Outline each Plasmodium ovale-infected red blood cell.
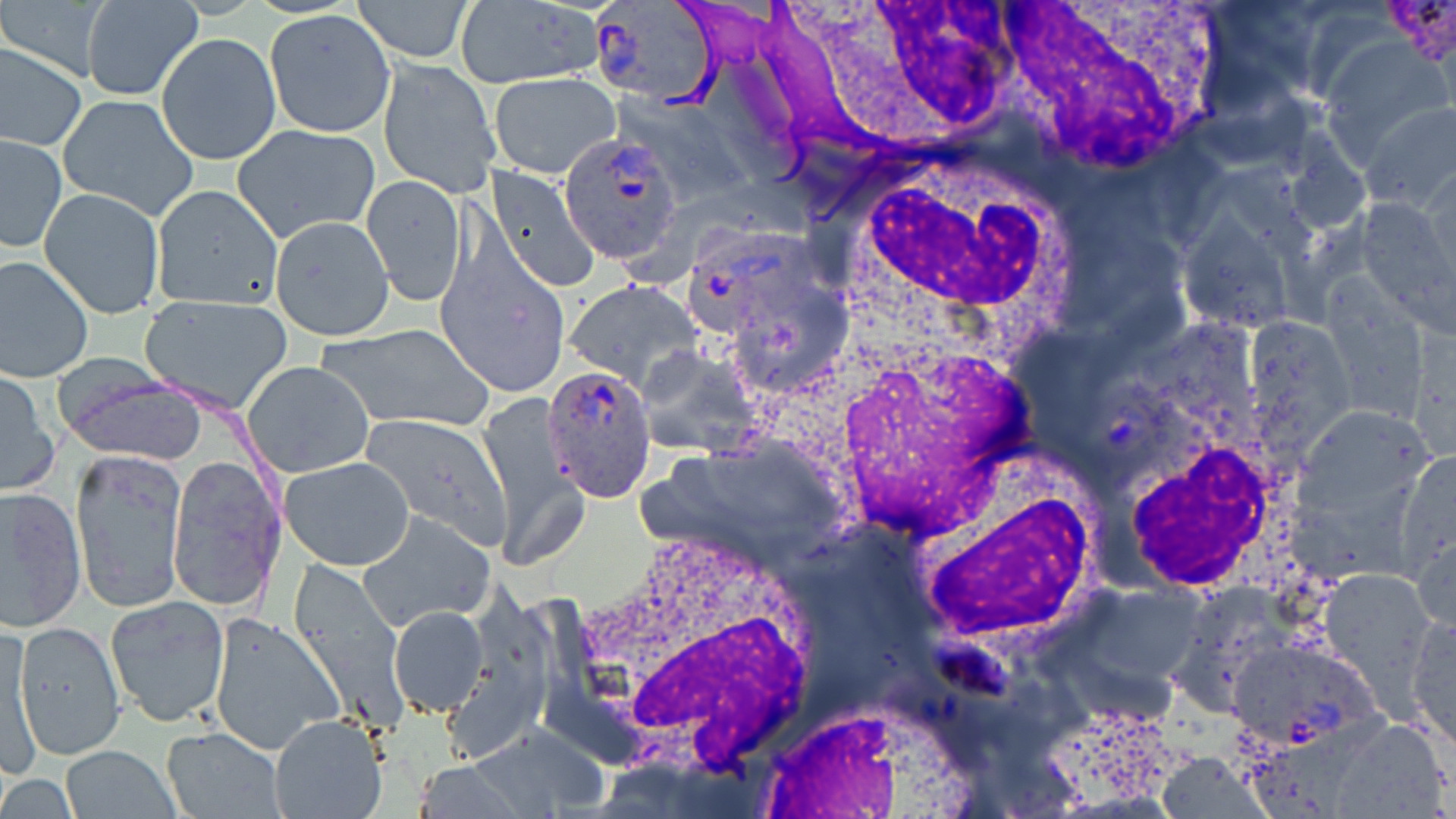
Approximate bounding boxes as (x1, y1, x2, y2) in pixels.
Plasmodium ovale-infected red blood cells: (588, 0, 719, 107), (557, 132, 683, 265), (681, 223, 824, 338), (540, 360, 656, 500).

White blood cell locations: (998, 0, 1234, 174), (803, 2, 1022, 133), (852, 155, 1067, 319), (816, 325, 1054, 545), (1116, 434, 1291, 591), (919, 442, 1100, 673), (570, 524, 826, 767), (743, 696, 989, 819). Uninfected red blood cell locations: (353, 0, 476, 63), (81, 1, 203, 101), (454, 2, 606, 88), (265, 10, 392, 136), (157, 32, 280, 165), (0, 42, 86, 151), (376, 57, 499, 195), (488, 72, 622, 180), (57, 93, 199, 220), (1358, 102, 1456, 212), (232, 124, 380, 244), (0, 134, 66, 251), (485, 166, 601, 291), (362, 174, 466, 306), (150, 184, 284, 312), (40, 186, 166, 320), (1174, 212, 1301, 335), (269, 216, 394, 341), (434, 243, 574, 391), (0, 254, 95, 382), (562, 280, 705, 391), (140, 296, 292, 411), (1242, 314, 1355, 457), (317, 322, 494, 432), (241, 359, 375, 480), (58, 367, 208, 464), (1, 368, 58, 495), (477, 395, 585, 572), (1298, 404, 1431, 520), (360, 413, 511, 548), (71, 449, 186, 612), (1398, 451, 1456, 572), (165, 454, 285, 613), (280, 457, 415, 570), (0, 486, 86, 633), (357, 511, 494, 632), (1410, 522, 1456, 637), (285, 564, 407, 729), (1321, 567, 1435, 695), (1043, 583, 1210, 720), (105, 595, 230, 726), (387, 605, 489, 716), (209, 613, 343, 753), (1407, 615, 1455, 752), (2, 620, 41, 777), (15, 620, 125, 759), (1223, 634, 1377, 751), (269, 714, 386, 819), (1324, 716, 1453, 817), (470, 722, 606, 817), (162, 726, 286, 818), (59, 746, 180, 819), (1157, 752, 1267, 819), (412, 761, 524, 818). Slide-level diagnosis: Plasmodium ovale. Captured at 1000x magnification. May-Grünwald-Giemsa-stained preparation. Thin blood smear. One field of a larger specimen. Optical microscopy. Image is 1456×819 pixels.